Classify this cell by malaria status.
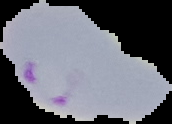
It is parasitized.

{
  "preparation": "thin blood film",
  "image_size": "172×124 pixels",
  "image_type": "cell region segmented out of the field of view; surrounding area masked to black"
}